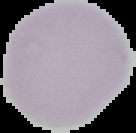
Summary:
  - Image size: 136×133 pixels
  - Preparation: thin blood smear
  - Malaria status: uninfected
  - Image type: segmented cell region with the area outside set to black